Name the parasite shown.
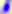
Toxoplasma gondii.

Photomicrograph. 400x magnification.